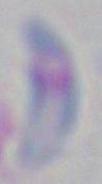 1000x magnification. Toxoplasma gondii is shown. Photomicrograph.